Give the position of every Plasmodium parasite.
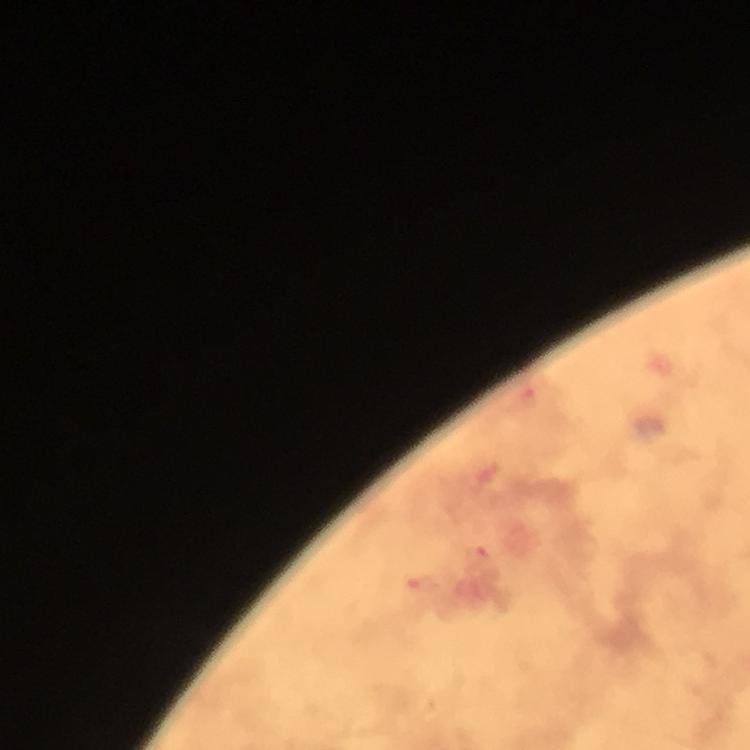

Approximate centers as [x, y] in pixels.
Plasmodium parasites: [529, 397], [481, 556], [419, 584].

cropped from = one field of view
context = from a diagnostic examination for malaria
image size = 750×750 pixels
stain = Giemsa
magnification = 100x
preparation = thick blood smear
immersion oil = applied
capture = smartphone mounted on the microscope